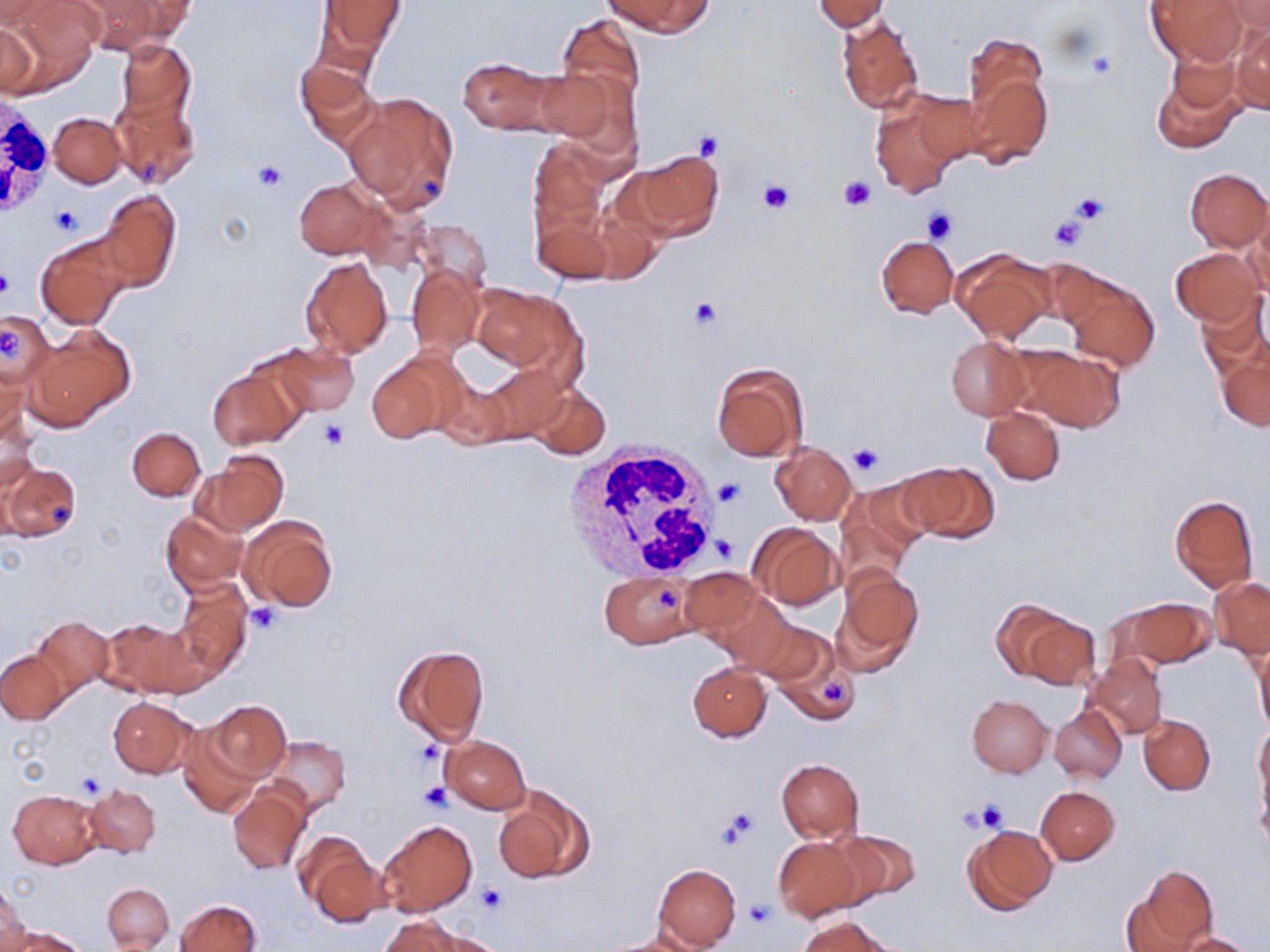

Summary:
  - Coordinate format: approximate bounding boxes as named x1/y1/x2/y2 corners in pixels
  - Platelet locations: (x1=1083, y1=46, x2=1117, y2=82), (x1=695, y1=131, x2=725, y2=160), (x1=252, y1=160, x2=289, y2=192), (x1=837, y1=175, x2=875, y2=210), (x1=755, y1=177, x2=796, y2=216), (x1=1071, y1=192, x2=1111, y2=226), (x1=51, y1=202, x2=82, y2=236), (x1=922, y1=206, x2=958, y2=245), (x1=1048, y1=215, x2=1087, y2=252), (x1=0, y1=264, x2=14, y2=301), (x1=687, y1=297, x2=723, y2=331), (x1=0, y1=325, x2=23, y2=362), (x1=317, y1=416, x2=350, y2=449), (x1=849, y1=444, x2=885, y2=477), (x1=714, y1=477, x2=747, y2=508), (x1=713, y1=534, x2=738, y2=564), (x1=245, y1=603, x2=283, y2=634), (x1=74, y1=770, x2=107, y2=799), (x1=417, y1=780, x2=452, y2=813), (x1=970, y1=801, x2=1010, y2=834), (x1=716, y1=807, x2=760, y2=850), (x1=476, y1=883, x2=506, y2=916), (x1=746, y1=899, x2=777, y2=927)
  - White blood cell locations: (x1=0, y1=92, x2=52, y2=219), (x1=564, y1=440, x2=722, y2=579)
  - Uninfected red blood cell locations: (x1=0, y1=0, x2=52, y2=29), (x1=11, y1=0, x2=101, y2=77), (x1=317, y1=0, x2=403, y2=64), (x1=607, y1=0, x2=711, y2=37), (x1=811, y1=0, x2=891, y2=31), (x1=1148, y1=0, x2=1246, y2=63), (x1=80, y1=1, x2=191, y2=51), (x1=1224, y1=2, x2=1270, y2=34), (x1=556, y1=15, x2=647, y2=110), (x1=837, y1=16, x2=925, y2=117), (x1=1232, y1=21, x2=1270, y2=115), (x1=0, y1=22, x2=42, y2=97), (x1=962, y1=32, x2=1048, y2=128), (x1=116, y1=39, x2=198, y2=129), (x1=459, y1=56, x2=576, y2=136), (x1=294, y1=60, x2=379, y2=150), (x1=1151, y1=63, x2=1244, y2=154), (x1=964, y1=64, x2=1052, y2=168), (x1=343, y1=90, x2=460, y2=212), (x1=111, y1=93, x2=201, y2=190), (x1=870, y1=95, x2=968, y2=197), (x1=48, y1=112, x2=127, y2=188), (x1=528, y1=139, x2=606, y2=231), (x1=628, y1=149, x2=724, y2=240), (x1=1184, y1=168, x2=1269, y2=253), (x1=293, y1=178, x2=389, y2=260), (x1=97, y1=189, x2=181, y2=291), (x1=533, y1=197, x2=615, y2=286), (x1=1244, y1=205, x2=1270, y2=294), (x1=414, y1=220, x2=494, y2=292), (x1=35, y1=234, x2=132, y2=330), (x1=876, y1=236, x2=958, y2=317), (x1=952, y1=247, x2=1054, y2=342), (x1=1170, y1=247, x2=1263, y2=327), (x1=299, y1=256, x2=395, y2=359), (x1=406, y1=263, x2=486, y2=355), (x1=1065, y1=277, x2=1159, y2=373), (x1=466, y1=283, x2=579, y2=376), (x1=1195, y1=292, x2=1270, y2=376), (x1=0, y1=309, x2=55, y2=388), (x1=27, y1=327, x2=133, y2=429), (x1=944, y1=336, x2=1030, y2=420), (x1=263, y1=342, x2=360, y2=418), (x1=1009, y1=344, x2=1124, y2=432), (x1=1218, y1=350, x2=1270, y2=431), (x1=367, y1=353, x2=461, y2=444), (x1=0, y1=363, x2=31, y2=447), (x1=711, y1=363, x2=809, y2=461), (x1=207, y1=366, x2=304, y2=451), (x1=528, y1=384, x2=611, y2=459), (x1=981, y1=407, x2=1065, y2=485), (x1=1, y1=414, x2=41, y2=500), (x1=127, y1=427, x2=204, y2=501), (x1=770, y1=443, x2=857, y2=525), (x1=195, y1=451, x2=288, y2=535), (x1=898, y1=461, x2=1001, y2=544), (x1=2, y1=462, x2=81, y2=543), (x1=847, y1=477, x2=938, y2=570), (x1=1169, y1=494, x2=1259, y2=591), (x1=161, y1=510, x2=247, y2=593), (x1=240, y1=515, x2=338, y2=612), (x1=749, y1=523, x2=841, y2=609), (x1=836, y1=567, x2=924, y2=668), (x1=679, y1=569, x2=764, y2=640), (x1=599, y1=573, x2=700, y2=648), (x1=1209, y1=575, x2=1270, y2=659), (x1=172, y1=578, x2=252, y2=678), (x1=710, y1=591, x2=794, y2=670), (x1=1119, y1=598, x2=1215, y2=670), (x1=993, y1=600, x2=1096, y2=689), (x1=32, y1=616, x2=113, y2=696), (x1=101, y1=617, x2=202, y2=698), (x1=752, y1=618, x2=843, y2=705), (x1=392, y1=644, x2=491, y2=746), (x1=1254, y1=644, x2=1270, y2=740), (x1=0, y1=651, x2=68, y2=724), (x1=1088, y1=654, x2=1167, y2=740), (x1=688, y1=663, x2=772, y2=742), (x1=967, y1=695, x2=1052, y2=776), (x1=107, y1=696, x2=196, y2=778), (x1=205, y1=700, x2=289, y2=779), (x1=1050, y1=705, x2=1127, y2=783), (x1=1139, y1=715, x2=1215, y2=794), (x1=1255, y1=722, x2=1269, y2=806), (x1=177, y1=725, x2=259, y2=816), (x1=440, y1=735, x2=530, y2=814), (x1=266, y1=736, x2=350, y2=815), (x1=775, y1=758, x2=865, y2=843), (x1=1257, y1=777, x2=1270, y2=852), (x1=492, y1=783, x2=595, y2=885), (x1=85, y1=784, x2=161, y2=858), (x1=229, y1=784, x2=310, y2=875), (x1=1036, y1=786, x2=1119, y2=865), (x1=10, y1=789, x2=101, y2=868), (x1=377, y1=819, x2=477, y2=918), (x1=962, y1=823, x2=1057, y2=914), (x1=838, y1=829, x2=921, y2=905), (x1=296, y1=832, x2=385, y2=928), (x1=771, y1=835, x2=864, y2=921), (x1=652, y1=864, x2=741, y2=949), (x1=1123, y1=866, x2=1216, y2=952), (x1=0, y1=882, x2=31, y2=952), (x1=102, y1=882, x2=173, y2=950), (x1=175, y1=900, x2=260, y2=952), (x1=377, y1=915, x2=482, y2=951), (x1=798, y1=916, x2=893, y2=952), (x1=9, y1=927, x2=92, y2=952), (x1=1178, y1=932, x2=1255, y2=952), (x1=600, y1=933, x2=705, y2=952)
  - Slide-level diagnosis: negative for blood parasites
  - Preparation: thin blood film
  - Magnification: 1000x
  - Stain: May-Grünwald-Giemsa
  - Field of view: one of a larger specimen
  - Image size: 1270×952 pixels
  - Modality: optical microscopy